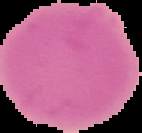 Segmented cell region on a black background. Image is 142×133 pixels. From a thin blood film. Malaria status: uninfected.